Locate every malaria parasite.
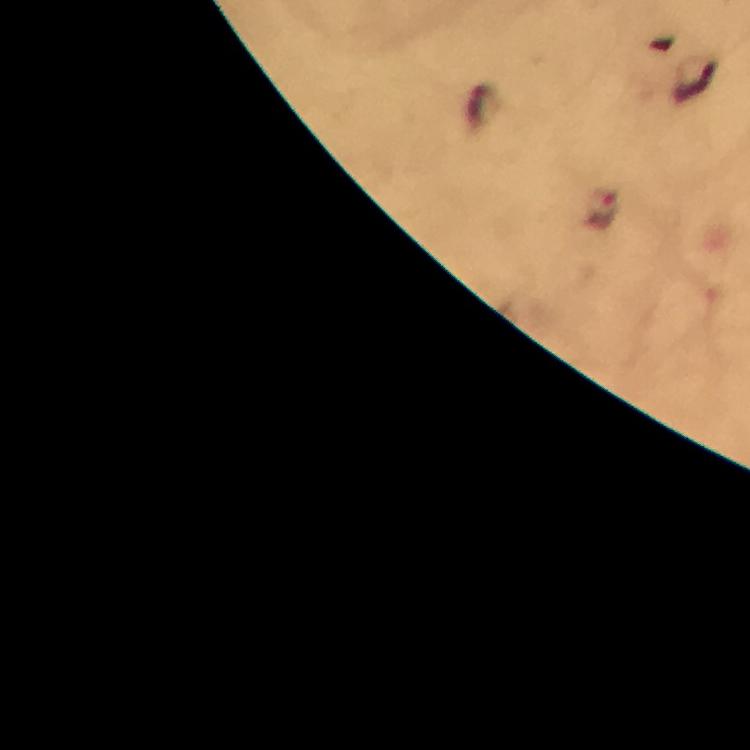

Approximate centers as (x, y) in pixels.
Malaria parasites: (606, 209).

Summary:
  - Immersion oil: applied
  - Preparation: thick smear
  - Capture: smartphone photograph through a microscope
  - Magnification: 100x
  - Cropped from: a single field of view
  - Stain: Giemsa
  - Image size: 750×750 pixels
  - Context: from a diagnostic examination for malaria